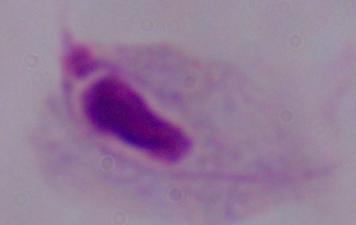
Summary:
  - Magnification: 1000x
  - Identification: trichomonad
  - Modality: micrograph